Classify this cell by malaria status.
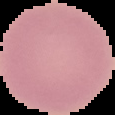

Uninfected.

Summary:
  - Image type: segmented cell region on a black background
  - Preparation: thin blood smear
  - Image size: 115×115 pixels